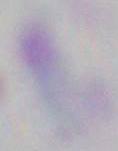

1000x magnification. Micrograph. Toxoplasma gondii is seen.